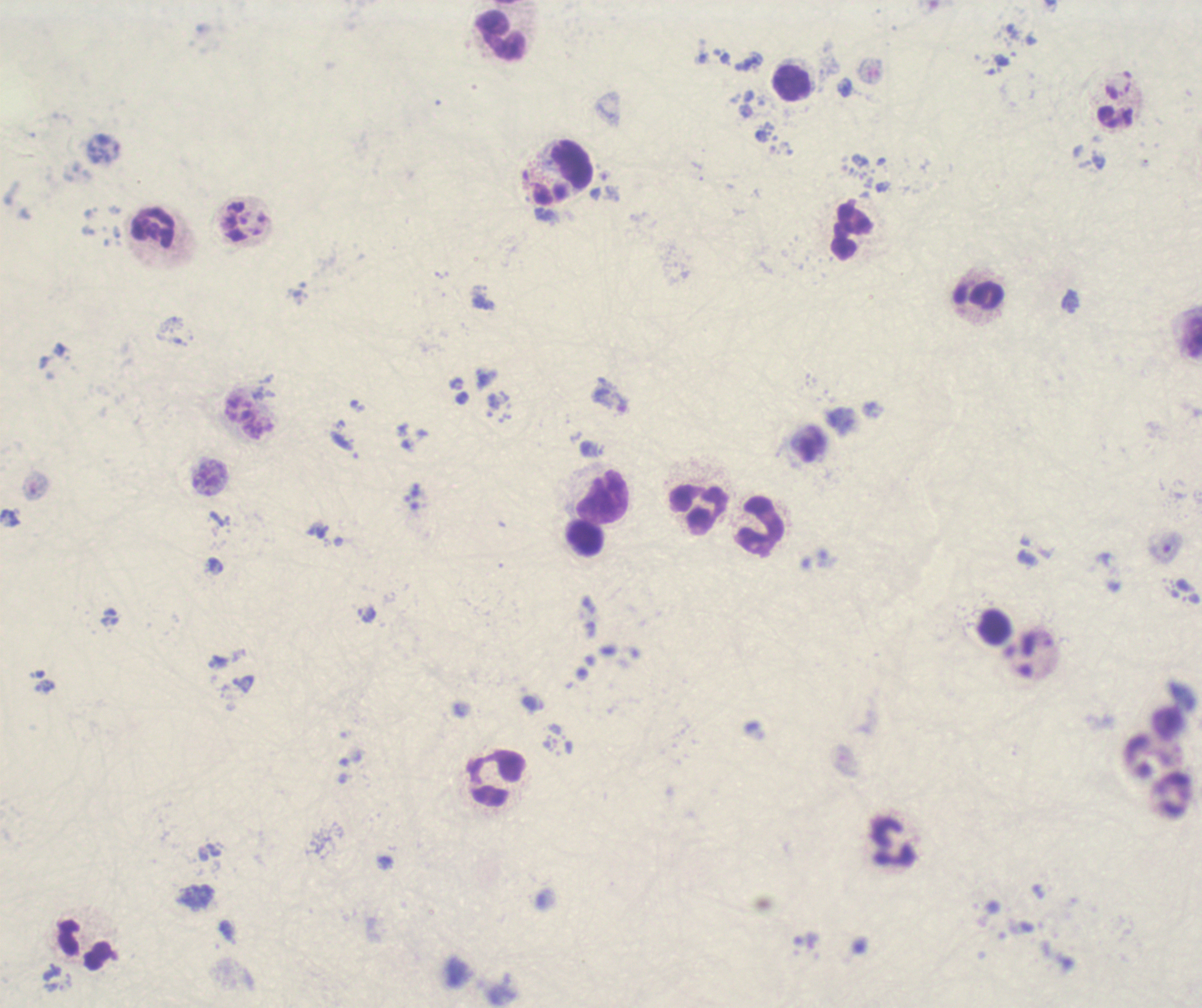

Approximate centers as [x, y] in pixels. Trophozoite locations: [608, 399]. Leukocyte locations: [501, 36], [792, 82], [571, 164], [154, 229], [852, 232], [977, 295], [604, 497], [698, 509], [761, 527], [585, 540], [995, 626], [495, 780], [892, 843], [86, 946]. Result: Plasmodium parasites detected. Image is 1202×1008 pixels. Captured at 100x magnification. Thick blood film. Romanowsky stain. Single field of view. Background quality: poor. Previously used in an actual diagnosis.